Assess this cell for malaria.
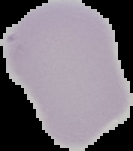
Uninfected.

image size = 133×151 pixels
image type = cell region segmented out of the field of view; surrounding area masked to black
preparation = thin blood smear